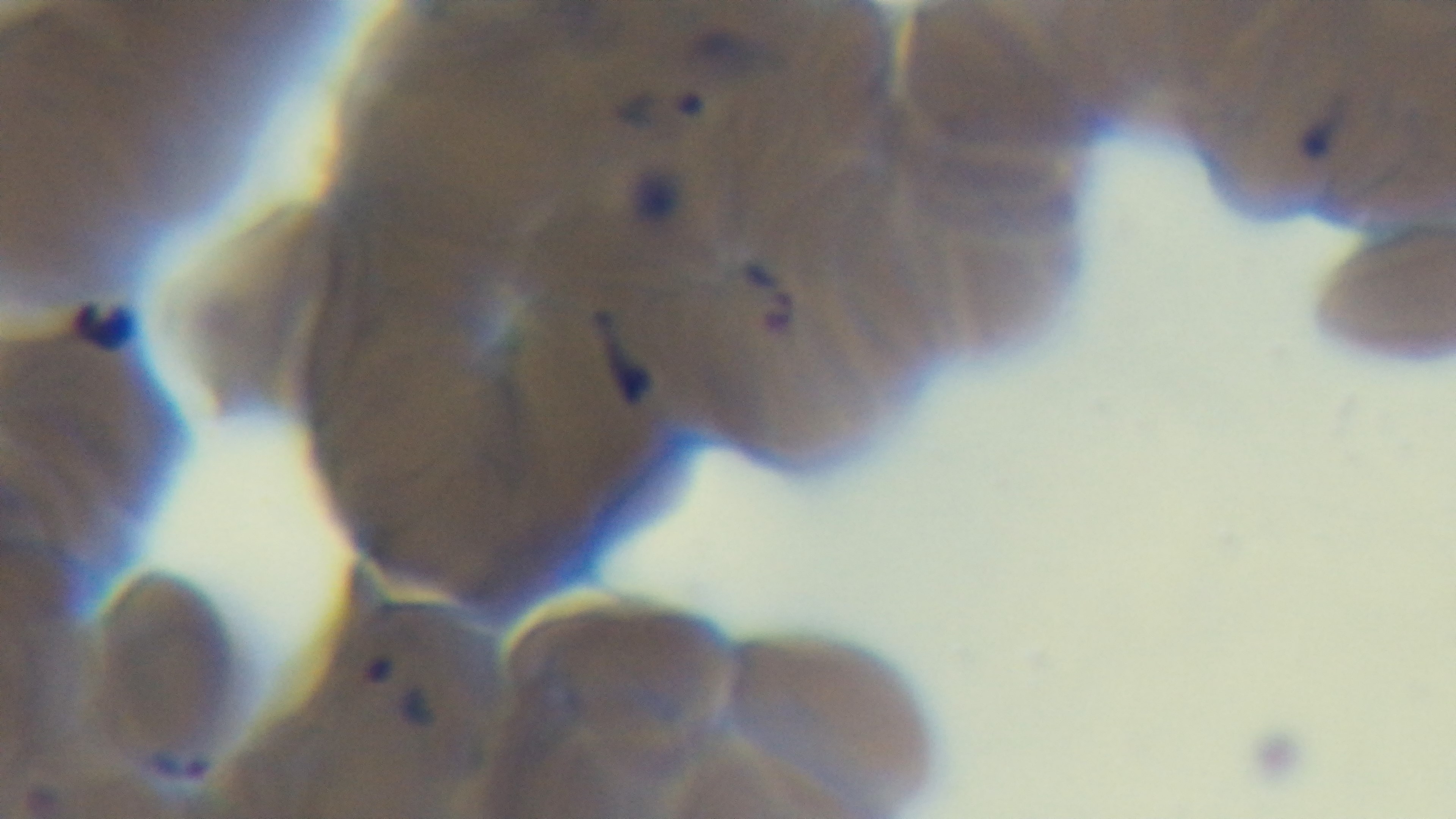

{
  "capture": "mounted 4K digital camera",
  "objective": "100x oil immersion",
  "field_of_view": "single",
  "modality": "light microscopy",
  "stain": "Giemsa",
  "preparation": "thin smear",
  "malaria_status": "infected"
}